Report the malaria status.
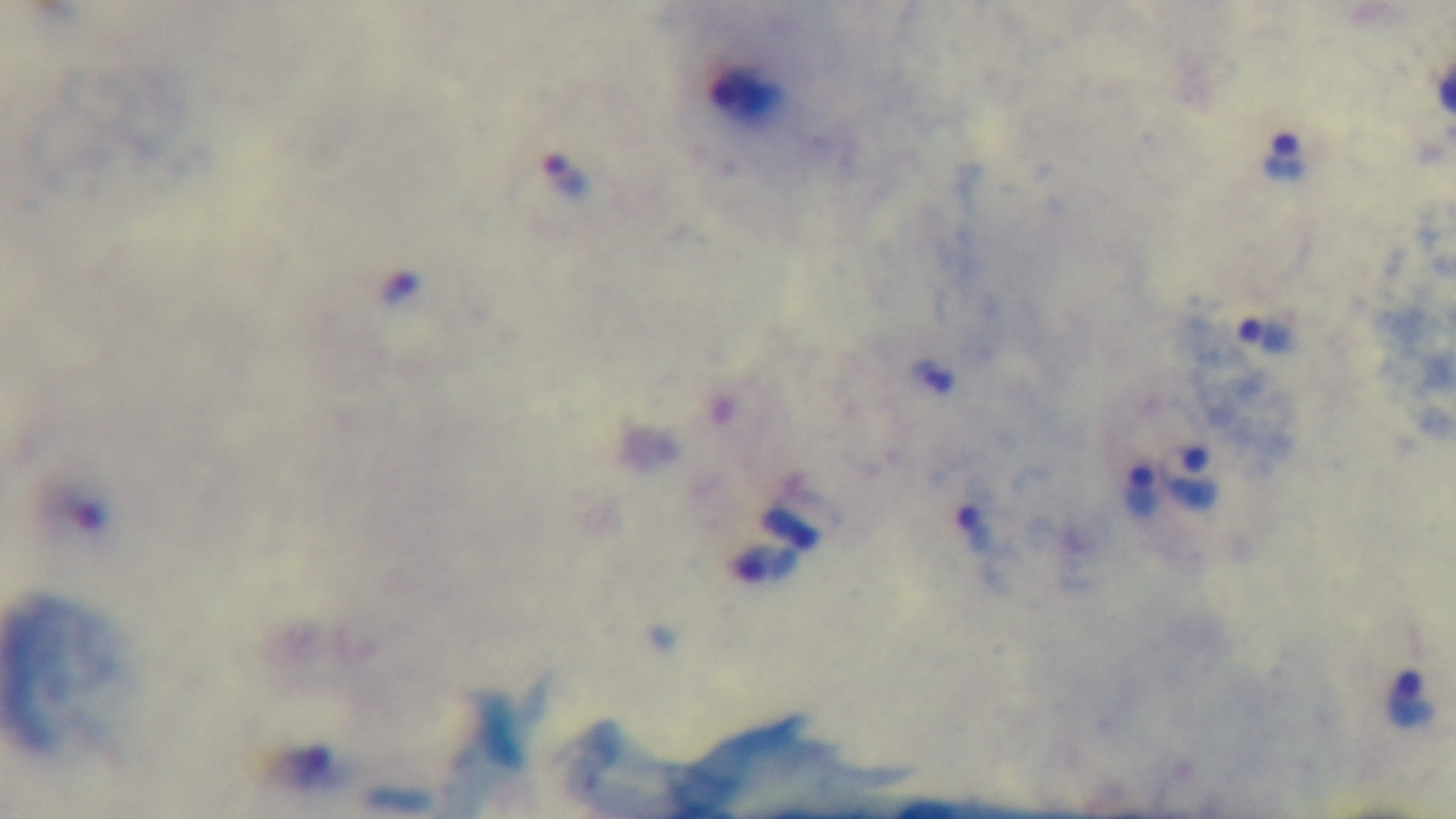
Positive.

capture: mounted 4K digital camera
modality: light microscopy
objective: 100x oil immersion
field_of_view: single
preparation: thick smear
stain: Giemsa